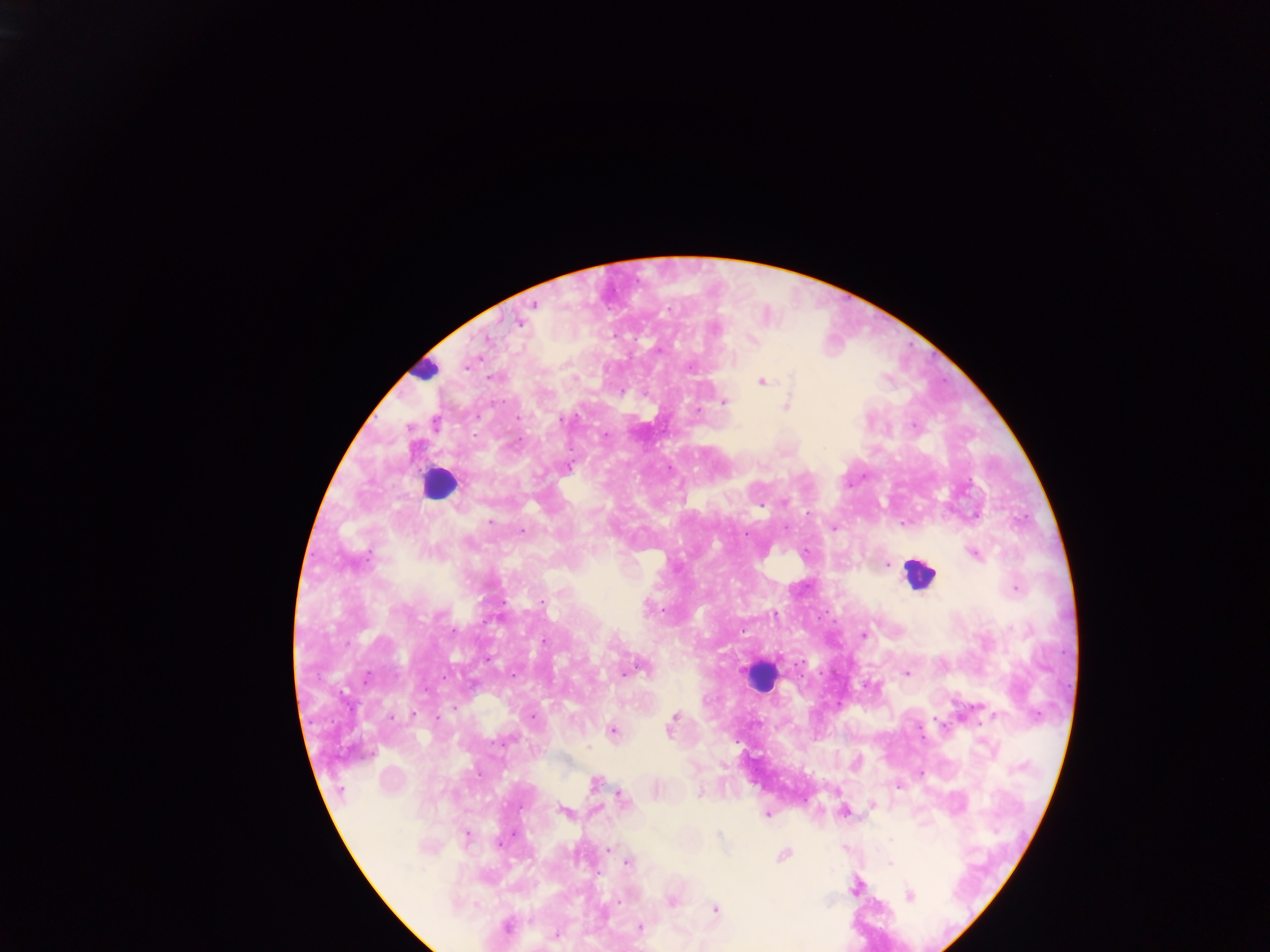

Approximate centers as x y in pixels.
Summary:
  - Leukocyte locations: 423 370; 439 484; 918 573; 760 676
  - Plasmodium parasite locations: 535 304; 520 321; 716 330; 487 340; 466 367; 690 368; 491 378; 761 382; 724 402; 787 405; 696 409; 519 418; 562 420; 435 423; 605 435; 569 466; 784 502; 490 522; 834 528; 523 531; 974 554; 887 565; 1016 589; 561 593; 648 609; 863 635; 543 642; 643 668; 631 671; 906 673; 514 675; 367 678; 414 714; 533 716; 675 716; 393 718; 671 728; 612 731; 588 747; 595 783; 700 793; 623 799; 563 811; 844 812; 767 814; 466 836; 609 849; 784 855; 627 863; 890 863; 855 887; 909 896; 672 900; 618 901; 716 908; 507 927; 640 928; 555 935
  - Field of view: single
  - Country: Ghana
  - Image size: 1270×952 pixels
  - Preparation: thick blood film
  - Capture: mobile-phone photograph through a microscope